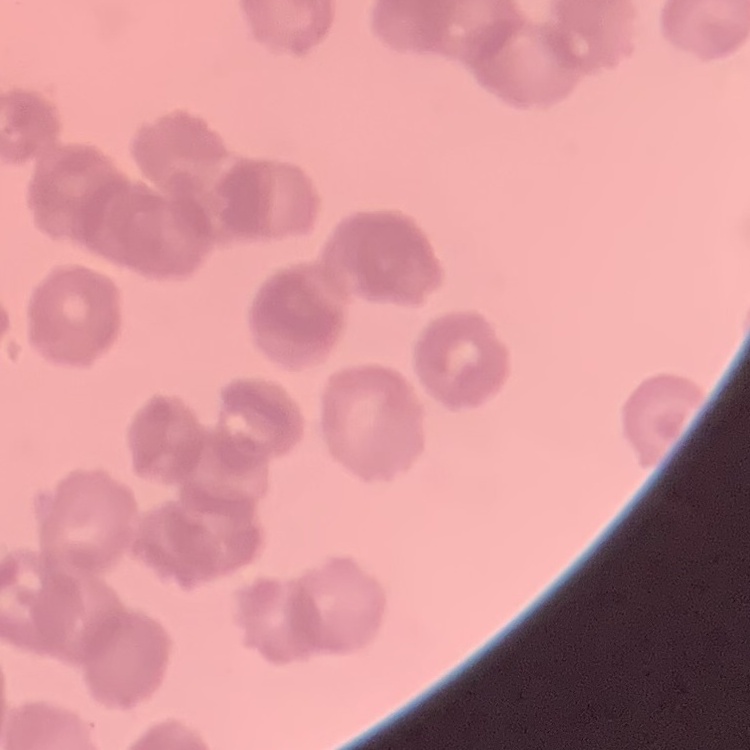

Summary:
  - Red blood cell morphology: rouleaux formation
  - Image type: square crop of a larger photomicrograph
  - Stain: Field's or Giemsa
  - Preparation: thin peripheral smear